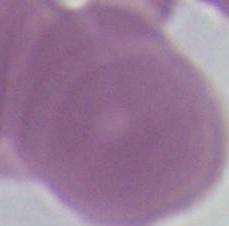
An erythrocyte is shown. Photomicrograph. 1000x magnification.